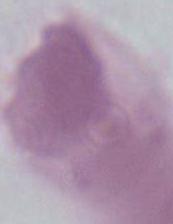
identification = red blood cell
modality = micrograph
magnification = 1000x